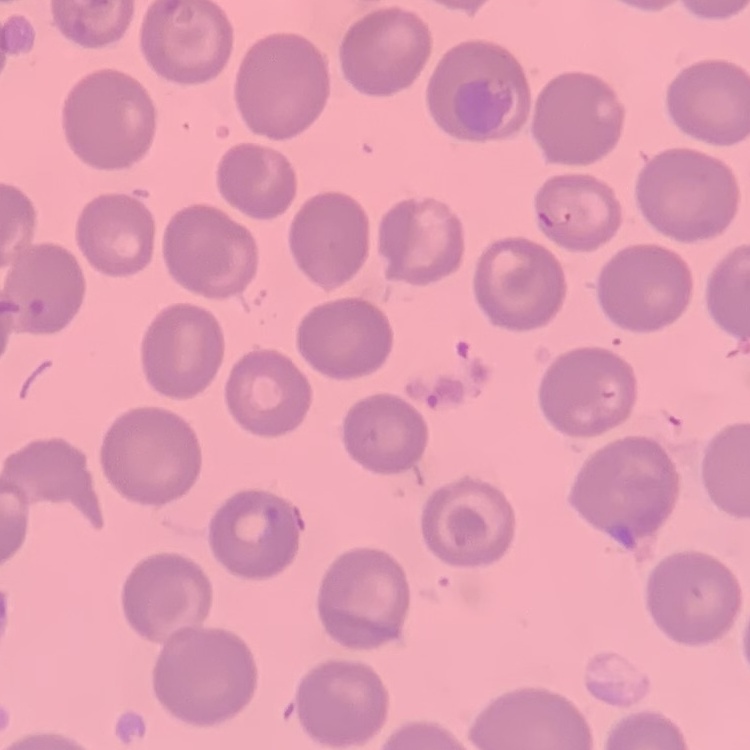
erythrocyte morphology = no rouleaux formation
stain = Field's or Giemsa
preparation = thin peripheral smear
image type = square crop of a larger photomicrograph